Assess this cell for malaria.
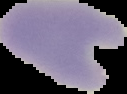

It is parasitized.

Summary:
  - Preparation: thin blood film
  - Image type: cell region segmented out of the field of view; surrounding area masked to black
  - Image size: 127×94 pixels